Classify this cell by malaria status.
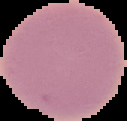

It is uninfected.

Summary:
  - Preparation: thin blood film
  - Image type: segmented cell region on a black background
  - Image size: 127×121 pixels